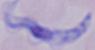

{
  "modality": "micrograph",
  "identification": "trypanosome",
  "magnification": "1000x"
}